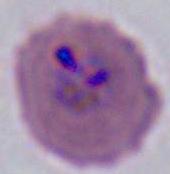

modality = micrograph
identification = Plasmodium
magnification = 400x or 1000x